Outline platelets.
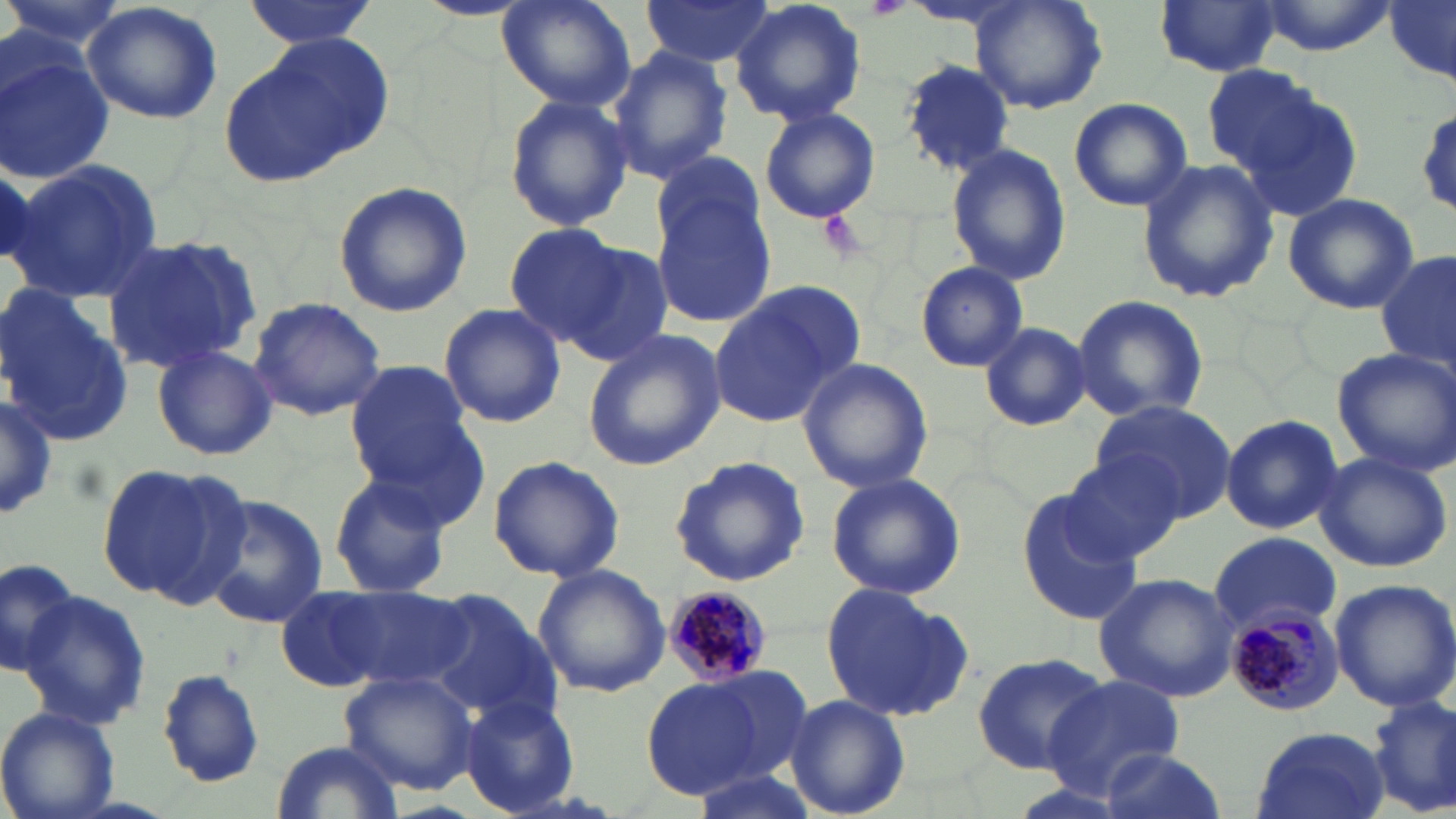
Approximate bounding boxes as [x1, y1, x2, y2] in pixels.
Platelets: [861, 0, 914, 22].

Plasmodium malariae-infected red blood cell locations: [664, 587, 778, 682], [1223, 606, 1343, 715]. Uninfected red blood cell locations: [1, 0, 123, 63], [241, 0, 379, 48], [411, 0, 531, 20], [496, 0, 635, 110], [637, 0, 777, 67], [729, 0, 869, 126], [1385, 0, 1456, 79], [972, 1, 1108, 115], [1153, 1, 1282, 77], [1253, 1, 1397, 54], [82, 2, 223, 125], [222, 32, 394, 186], [1, 45, 116, 185], [606, 48, 732, 182], [899, 60, 1017, 176], [1203, 66, 1321, 173], [1238, 85, 1364, 222], [504, 94, 634, 234], [1067, 97, 1194, 212], [758, 105, 882, 225], [945, 143, 1069, 286], [6, 159, 163, 302], [1136, 160, 1279, 305], [332, 181, 474, 319], [651, 184, 775, 326], [1283, 193, 1419, 314], [502, 224, 630, 346], [98, 231, 263, 373], [558, 239, 674, 365], [1378, 249, 1455, 374], [915, 262, 1029, 372], [0, 283, 136, 446], [710, 285, 860, 429], [1070, 294, 1209, 425], [248, 296, 387, 422], [438, 303, 566, 428], [980, 323, 1092, 430], [580, 327, 727, 473], [151, 342, 276, 460], [1332, 345, 1456, 473], [798, 356, 932, 492], [345, 361, 479, 499], [0, 396, 60, 520], [1090, 400, 1240, 524], [1220, 414, 1344, 534], [1312, 449, 1453, 573], [1059, 452, 1188, 565], [485, 455, 624, 582], [667, 455, 811, 588], [95, 460, 245, 606], [327, 471, 452, 599], [826, 471, 967, 602], [1017, 489, 1142, 626], [200, 494, 327, 627], [1209, 531, 1342, 634], [0, 557, 79, 678], [532, 563, 671, 698], [1093, 571, 1242, 703], [1328, 577, 1456, 712], [819, 581, 975, 724], [302, 582, 472, 693], [19, 589, 150, 730], [424, 590, 558, 720], [969, 651, 1113, 775], [684, 663, 814, 788], [338, 666, 481, 795], [156, 667, 266, 788], [1045, 676, 1184, 794], [642, 678, 768, 799], [460, 692, 580, 817], [783, 694, 910, 819], [1367, 696, 1454, 818], [0, 707, 119, 819], [1250, 726, 1390, 819], [270, 738, 402, 819], [1092, 748, 1229, 819]. Slide-level diagnosis: Plasmodium malariae. Optical microscopy. Captured at 1000x magnification. Thin blood film. One field of a larger specimen. Image is 1456×819 pixels. May-Grünwald-Giemsa-stained preparation.